Point out each Plasmodium parasite.
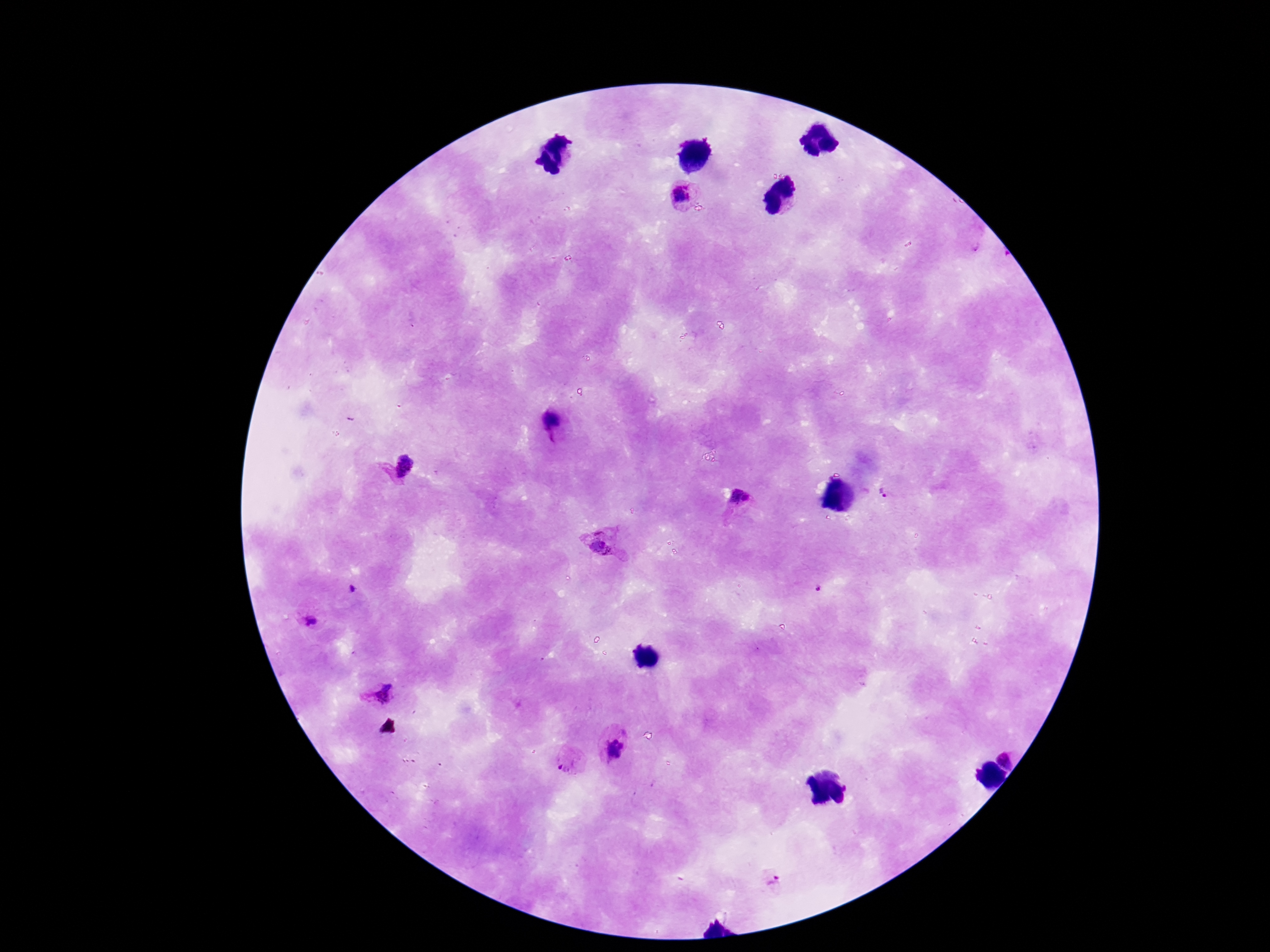
Approximate object centers, in pixels from the top-left corner.
Plasmodium parasites: (x=684, y=194), (x=552, y=421), (x=404, y=465), (x=742, y=499), (x=598, y=544), (x=352, y=589), (x=310, y=617), (x=380, y=694), (x=615, y=749), (x=1009, y=756), (x=568, y=763), (x=772, y=881).

Giemsa-stained preparation. Patient malaria status: infected. Image is 1270×952 pixels. Thick blood film. 100x magnification. Photographed through the microscope eyepiece with a smartphone camera. One field from this slide.